Name the cell type shown.
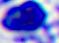
This is a leukocyte.

Captured at 400x magnification. Micrograph.